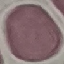
malaria_status: uninfected
capture: smartphone through the microscope eyepiece
stain: Giemsa
image_type: cell patch, automatically extracted from a larger field of view and resized to 64 × 64 pixels
preparation: thin smear